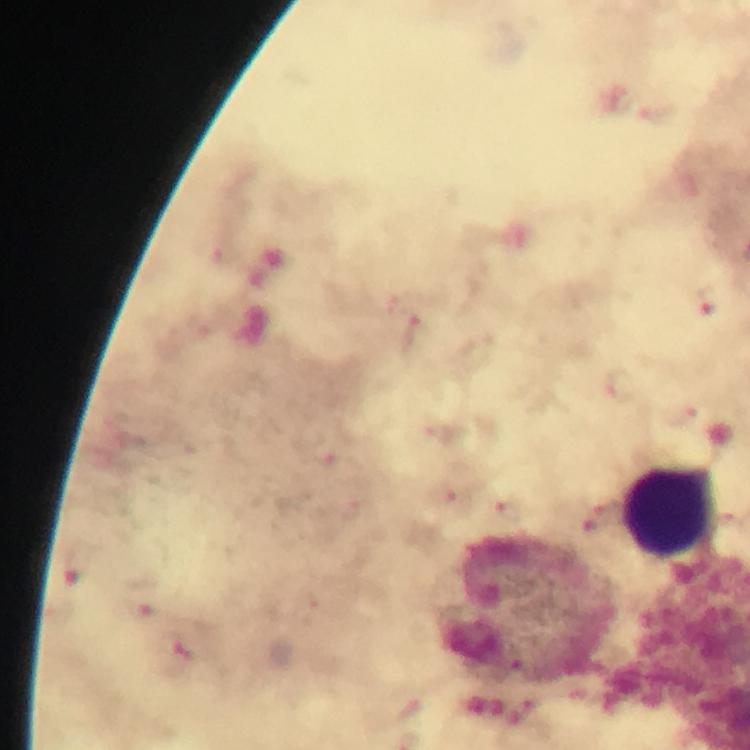

context = from a diagnostic examination for malaria
stain = Giemsa
magnification = 100x
image size = 750×750 pixels
leukocyte locations = approximate centers as (x, y) in pixels: (669, 511)
capture = smartphone mounted on the microscope
preparation = thick blood smear
immersion oil = used
cropped from = one field of view
malaria parasite locations = approximate centers as (x, y) in pixels: (225, 253), (706, 301), (416, 333), (623, 385), (684, 416), (325, 451), (446, 494), (511, 512), (598, 518), (78, 566), (138, 599), (184, 658)